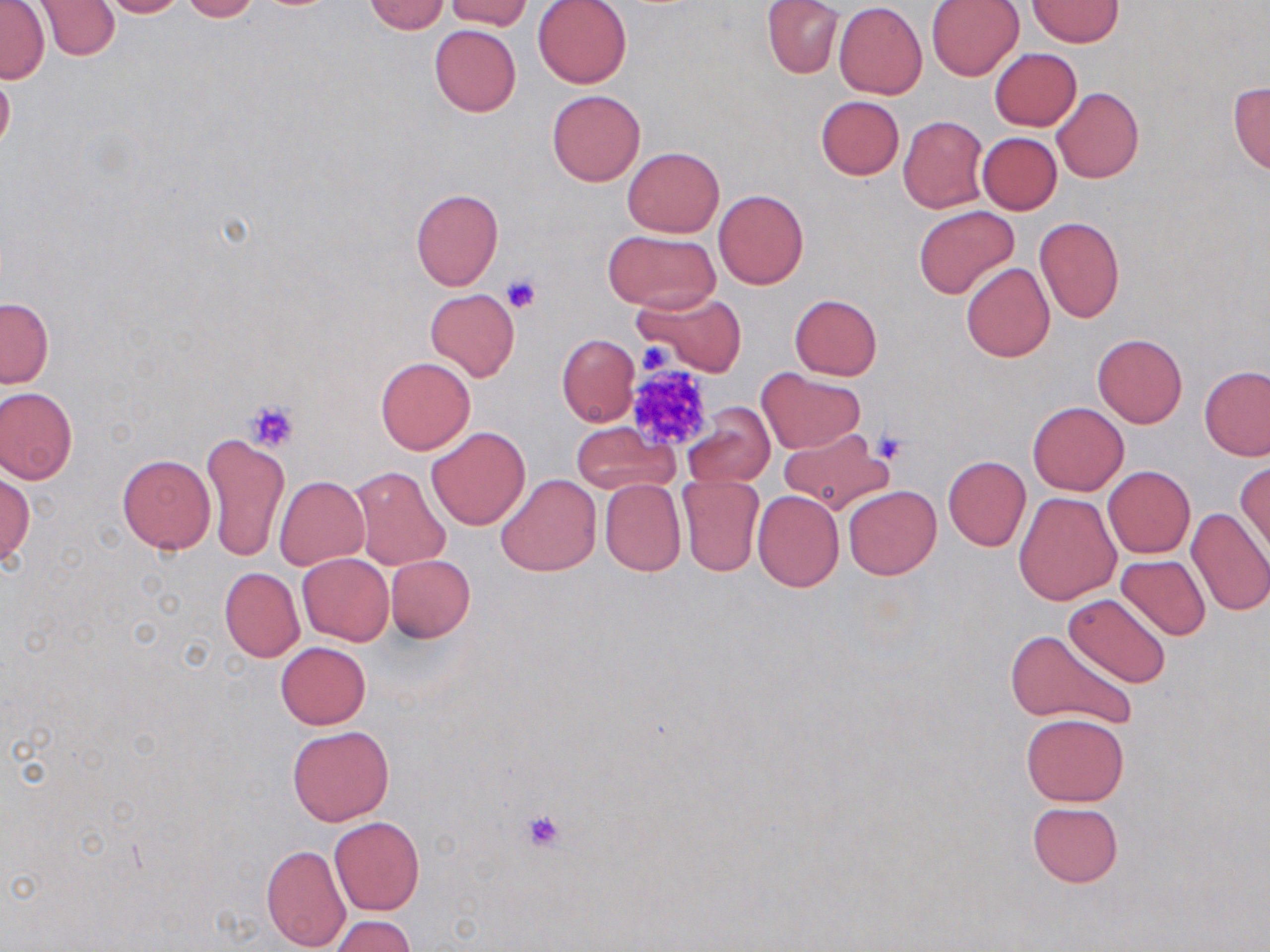

slide-level diagnosis = no evidence of blood parasites
modality = light microscopy
preparation = thin blood smear
uninfected red blood cell locations = approximate bounding boxes as (x1, y1, x2, y2) in pixels: (34, 0, 122, 62), (100, 0, 191, 19), (179, 0, 260, 21), (445, 0, 531, 30), (532, 0, 632, 88), (762, 0, 843, 78), (926, 0, 1025, 81), (365, 1, 450, 34), (1028, 1, 1123, 47), (834, 2, 927, 99), (1, 3, 50, 84), (429, 23, 522, 117), (990, 48, 1081, 130), (0, 64, 15, 159), (1228, 82, 1270, 176), (1052, 86, 1144, 183), (547, 89, 646, 186), (815, 96, 905, 180), (899, 115, 989, 213), (978, 133, 1062, 214), (622, 147, 725, 237), (410, 187, 503, 290), (713, 189, 809, 289), (913, 207, 1020, 299), (1034, 216, 1125, 323), (603, 230, 719, 313), (991, 239, 1110, 347), (960, 263, 1055, 362), (425, 289, 520, 381), (633, 290, 747, 376), (789, 294, 883, 380), (0, 297, 52, 387), (1091, 333, 1188, 428), (557, 334, 639, 426), (376, 357, 474, 454), (1200, 366, 1269, 462), (755, 368, 865, 454), (0, 387, 78, 485), (1027, 400, 1129, 495), (682, 404, 775, 489), (571, 422, 679, 495), (426, 426, 531, 529), (776, 428, 894, 517), (201, 432, 289, 562), (117, 454, 216, 554), (943, 456, 1031, 550), (1237, 461, 1270, 559), (1103, 465, 1195, 558), (349, 466, 450, 571), (1, 472, 34, 566), (495, 474, 601, 577), (275, 475, 368, 568), (676, 475, 766, 578), (598, 479, 685, 575), (843, 486, 941, 580), (753, 489, 844, 590), (1013, 491, 1122, 605), (1185, 506, 1270, 617), (296, 553, 393, 645), (386, 555, 475, 642), (1115, 555, 1211, 641), (219, 567, 305, 662), (1064, 593, 1172, 688), (1005, 630, 1137, 730), (275, 642, 370, 729), (1020, 712, 1130, 805), (288, 724, 394, 825), (1027, 801, 1124, 887), (329, 816, 425, 916), (261, 843, 351, 950), (331, 915, 415, 952)
field of view = single
stain = May-Grünwald-Giemsa
platelet locations = approximate bounding boxes as (x1, y1, x2, y2) in pixels: (500, 274, 542, 313), (636, 343, 675, 376), (626, 363, 717, 450), (243, 399, 301, 453), (872, 430, 910, 464), (520, 808, 570, 853)
magnification = 1000x
image size = 1270×952 pixels